Name the parasite shown.
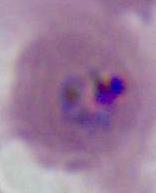

Plasmodium.

Captured at either 400x or 1000x magnification. Micrograph.